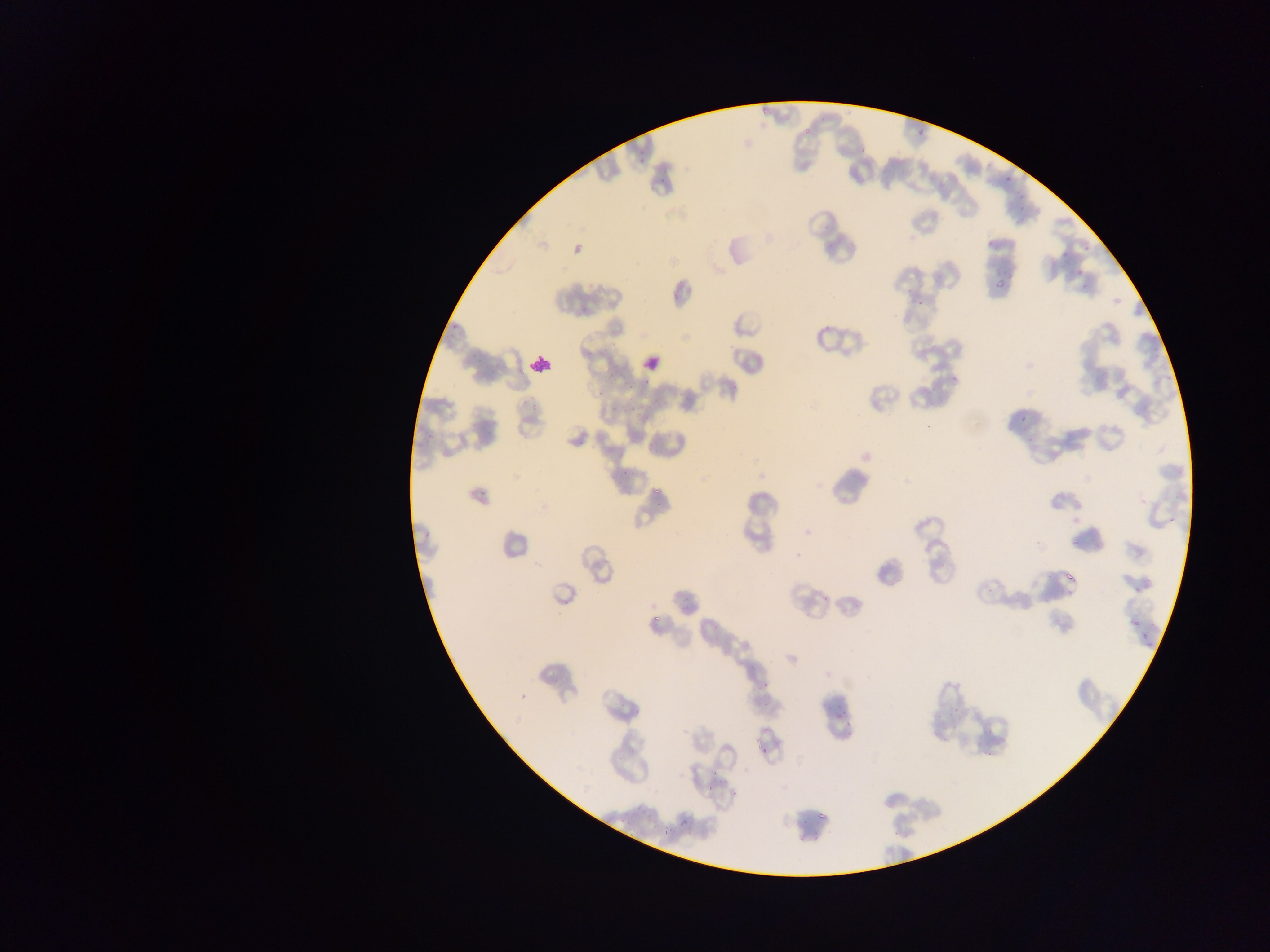
Approximate bounding boxes as (left, top, right, bottom) in pixels.
Summary:
  - Plasmodium parasite locations: (760, 107, 772, 118), (802, 126, 811, 136), (917, 128, 925, 136), (858, 138, 874, 154), (639, 151, 651, 162), (1003, 176, 1011, 183), (659, 178, 668, 185), (1015, 193, 1026, 200), (1013, 219, 1023, 226), (988, 238, 995, 249), (1060, 254, 1068, 261), (991, 268, 1018, 292), (1075, 268, 1086, 277), (672, 292, 680, 300), (917, 293, 927, 306), (450, 324, 462, 337), (467, 352, 481, 360), (607, 368, 622, 380), (950, 375, 958, 382), (643, 378, 650, 386), (627, 380, 638, 391), (597, 390, 603, 401), (651, 394, 660, 406), (528, 401, 539, 414), (609, 404, 618, 416), (631, 404, 640, 412), (1018, 415, 1029, 422), (485, 430, 496, 437), (646, 438, 658, 451), (577, 440, 585, 446), (623, 465, 633, 479), (652, 479, 663, 498), (480, 487, 490, 499), (1071, 539, 1078, 547), (1061, 573, 1080, 590), (1135, 587, 1147, 592), (563, 599, 569, 607), (1132, 614, 1143, 623), (650, 617, 661, 628), (712, 624, 722, 630), (1141, 638, 1155, 652), (761, 676, 775, 687), (950, 707, 963, 720), (836, 710, 848, 720), (948, 726, 957, 735), (844, 732, 851, 740), (756, 744, 766, 757), (986, 751, 994, 758), (712, 771, 721, 779), (819, 805, 827, 819), (622, 813, 639, 830), (648, 817, 655, 827), (679, 819, 691, 828), (661, 831, 676, 837) | approximate (x, y) pixel centers of objects too small to bound: (1088, 247), (606, 348), (991, 592)
  - Leukocyte locations: (640, 350, 666, 376), (531, 353, 555, 375)
  - Country: Ghana
  - Image size: 1270×952 pixels
  - Preparation: thin blood film
  - Capture: mobile-phone photograph through a microscope
  - Field of view: single